Report the malaria status of this cell.
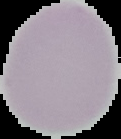

Uninfected.

image type = segmented cell region with the area outside set to black
preparation = thin blood film
image size = 121×139 pixels